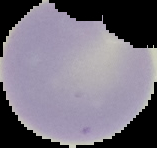
preparation: thin blood smear
image_type: cell region segmented out of the field of view; surrounding area masked to black
image_size: 157×148 pixels
malaria_status: uninfected